Assess for Plasmodium parasites.
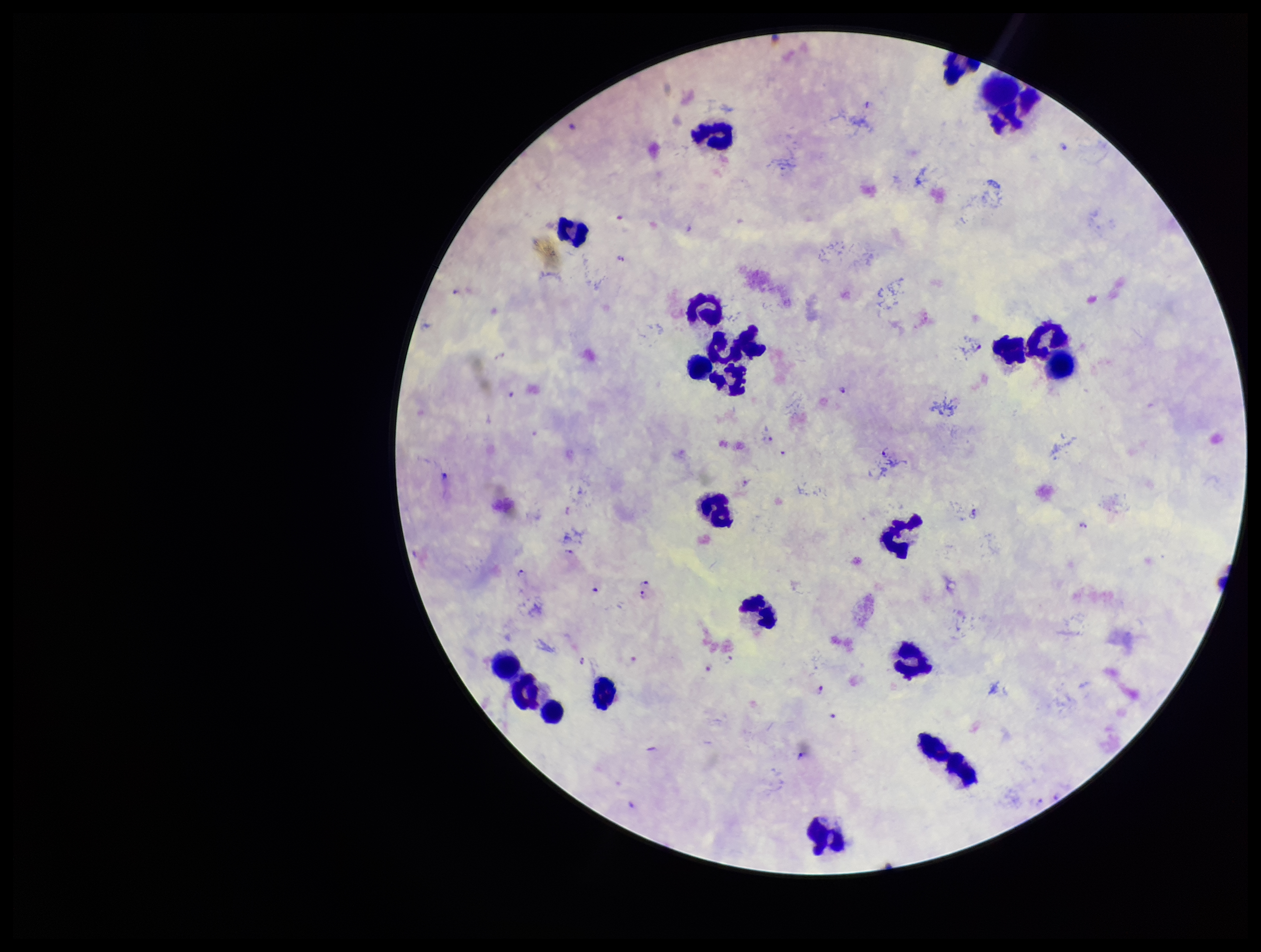
Seen.

{
  "leukocyte_count": 21,
  "preparation": "thick smear",
  "stain": "Giemsa",
  "image_size": "1261×952 pixels",
  "field_of_view": "one from this slide",
  "capture": "smartphone photograph through the microscope eyepiece",
  "parasite_count": 16,
  "patient_malaria_status": "positive",
  "species_reported_for_this_patient": "Plasmodium falciparum"
}